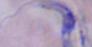
Summary:
  - Identification: trypanosome
  - Magnification: 1000x
  - Modality: photomicrograph